Classify this cell by malaria status.
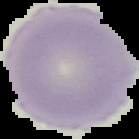

It is parasitized.

{
  "preparation": "thin blood smear",
  "image_size": "139×139 pixels",
  "image_type": "segmented cell region on a black background"
}